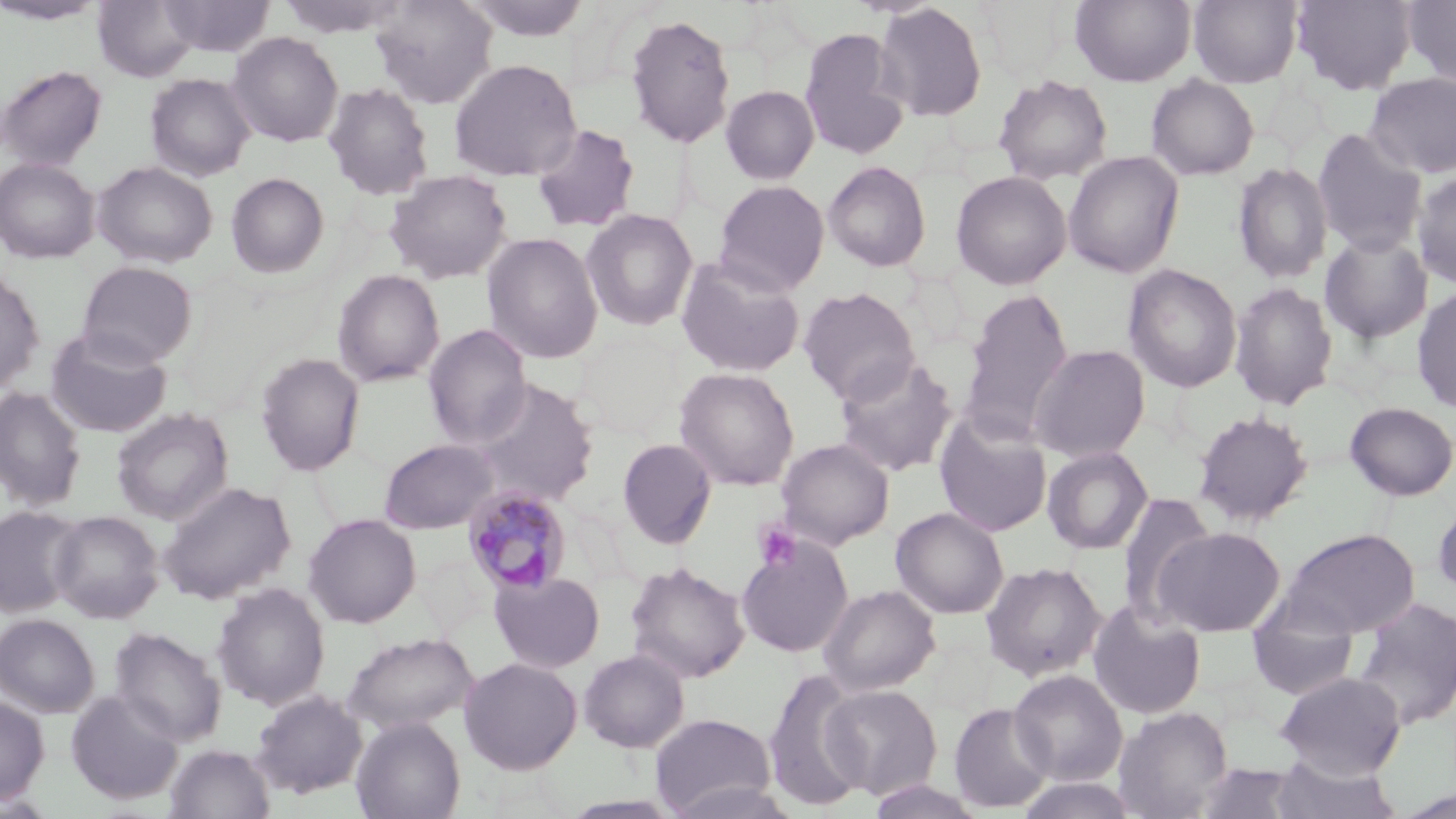 Approximate bounding boxes as named x1/y1/x2/y2 corners in pixels. Uninfected red blood cell locations: (x1=0, y1=0, x2=109, y2=26), (x1=93, y1=0, x2=200, y2=82), (x1=159, y1=0, x2=274, y2=56), (x1=276, y1=0, x2=409, y2=38), (x1=370, y1=0, x2=497, y2=109), (x1=462, y1=0, x2=594, y2=42), (x1=1070, y1=0, x2=1196, y2=87), (x1=1188, y1=0, x2=1302, y2=88), (x1=1291, y1=0, x2=1417, y2=93), (x1=1402, y1=0, x2=1456, y2=89), (x1=873, y1=2, x2=988, y2=122), (x1=623, y1=12, x2=736, y2=149), (x1=799, y1=27, x2=910, y2=160), (x1=227, y1=32, x2=344, y2=146), (x1=448, y1=58, x2=582, y2=182), (x1=0, y1=64, x2=107, y2=171), (x1=1364, y1=72, x2=1456, y2=180), (x1=145, y1=73, x2=256, y2=181), (x1=993, y1=74, x2=1113, y2=185), (x1=1146, y1=75, x2=1259, y2=180), (x1=322, y1=81, x2=435, y2=201), (x1=721, y1=85, x2=819, y2=184), (x1=531, y1=123, x2=640, y2=233), (x1=1312, y1=128, x2=1427, y2=256), (x1=1064, y1=151, x2=1184, y2=277), (x1=0, y1=157, x2=99, y2=263), (x1=823, y1=160, x2=932, y2=271), (x1=93, y1=161, x2=218, y2=268), (x1=1232, y1=162, x2=1334, y2=284), (x1=385, y1=169, x2=512, y2=284), (x1=951, y1=170, x2=1072, y2=290), (x1=1412, y1=171, x2=1456, y2=289), (x1=226, y1=172, x2=329, y2=278), (x1=714, y1=180, x2=830, y2=296), (x1=581, y1=209, x2=699, y2=331), (x1=482, y1=232, x2=603, y2=364), (x1=1320, y1=232, x2=1434, y2=344), (x1=676, y1=256, x2=806, y2=378), (x1=77, y1=261, x2=197, y2=368), (x1=1123, y1=264, x2=1243, y2=393), (x1=0, y1=268, x2=44, y2=395), (x1=331, y1=269, x2=445, y2=388), (x1=1229, y1=281, x2=1339, y2=410), (x1=1412, y1=286, x2=1456, y2=414), (x1=798, y1=287, x2=921, y2=405), (x1=960, y1=288, x2=1075, y2=444), (x1=422, y1=324, x2=532, y2=449), (x1=45, y1=328, x2=173, y2=438), (x1=1029, y1=344, x2=1151, y2=463), (x1=255, y1=352, x2=366, y2=476), (x1=833, y1=354, x2=958, y2=478), (x1=674, y1=367, x2=800, y2=491), (x1=470, y1=379, x2=600, y2=507), (x1=0, y1=386, x2=87, y2=511), (x1=1345, y1=402, x2=1456, y2=500), (x1=111, y1=408, x2=234, y2=525), (x1=934, y1=409, x2=1053, y2=537), (x1=1192, y1=409, x2=1313, y2=526), (x1=618, y1=438, x2=717, y2=549), (x1=775, y1=438, x2=894, y2=550), (x1=378, y1=439, x2=500, y2=534), (x1=1041, y1=446, x2=1153, y2=555), (x1=158, y1=481, x2=296, y2=604), (x1=1116, y1=493, x2=1218, y2=624), (x1=1432, y1=497, x2=1456, y2=602), (x1=0, y1=507, x2=82, y2=617), (x1=892, y1=507, x2=1009, y2=619), (x1=49, y1=510, x2=163, y2=623), (x1=303, y1=513, x2=421, y2=628), (x1=1154, y1=526, x2=1285, y2=636), (x1=1279, y1=528, x2=1419, y2=638), (x1=736, y1=535, x2=853, y2=658), (x1=624, y1=561, x2=750, y2=684), (x1=980, y1=562, x2=1106, y2=681), (x1=489, y1=571, x2=606, y2=673), (x1=211, y1=583, x2=330, y2=711), (x1=818, y1=583, x2=940, y2=696), (x1=1352, y1=596, x2=1456, y2=730), (x1=1087, y1=600, x2=1206, y2=720), (x1=1246, y1=604, x2=1360, y2=701), (x1=0, y1=614, x2=99, y2=718), (x1=110, y1=626, x2=227, y2=746), (x1=343, y1=632, x2=479, y2=733), (x1=578, y1=648, x2=690, y2=753), (x1=459, y1=657, x2=582, y2=774), (x1=762, y1=668, x2=871, y2=812), (x1=1009, y1=670, x2=1127, y2=786), (x1=1275, y1=671, x2=1407, y2=779), (x1=821, y1=684, x2=943, y2=800), (x1=65, y1=689, x2=185, y2=805), (x1=250, y1=690, x2=368, y2=799), (x1=0, y1=695, x2=49, y2=805), (x1=949, y1=702, x2=1055, y2=813), (x1=1113, y1=705, x2=1233, y2=819), (x1=649, y1=713, x2=777, y2=817), (x1=350, y1=716, x2=466, y2=819), (x1=165, y1=744, x2=275, y2=819), (x1=1270, y1=757, x2=1402, y2=819), (x1=1195, y1=762, x2=1305, y2=819), (x1=1015, y1=775, x2=1143, y2=819), (x1=663, y1=779, x2=803, y2=819), (x1=864, y1=779, x2=988, y2=818). Plasmodium malariae-infected red blood cell locations: (x1=462, y1=485, x2=573, y2=597). Platelet locations: (x1=753, y1=520, x2=802, y2=572). Slide-level diagnosis: Plasmodium malariae. Single field of view. Thin blood film. May-Grünwald-Giemsa-stained preparation. Captured at 1000x magnification. Image is 1456×819 pixels. Light microscopy.